Point out every Plasmodium parasite.
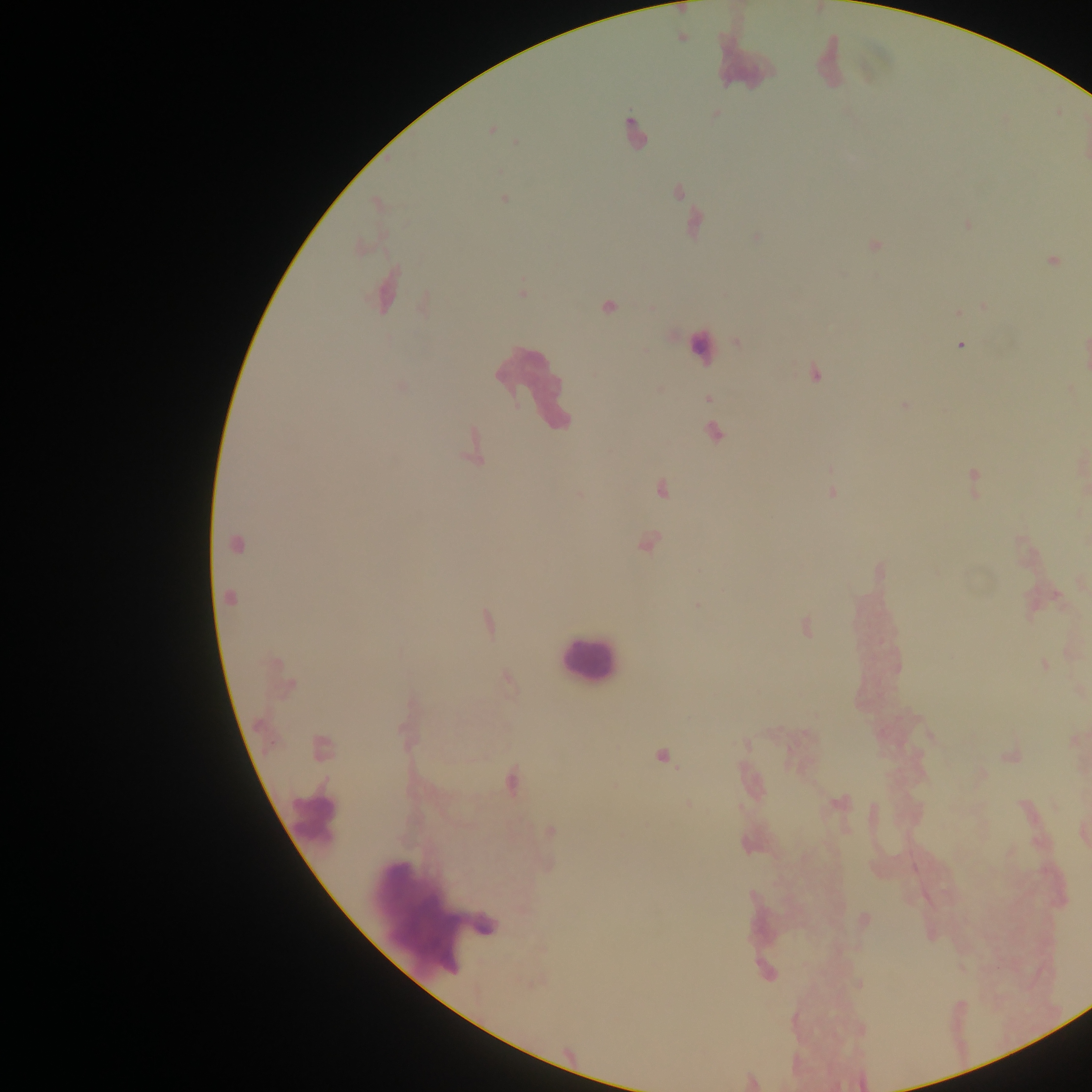
Approximate centers as [x, y] in pixels.
Plasmodium parasites: [492, 130], [504, 198], [1053, 261], [958, 312], [960, 345], [815, 373], [708, 399], [714, 433], [973, 482], [661, 487], [647, 543], [236, 544], [879, 572], [229, 597], [696, 606], [488, 623], [806, 626], [1045, 665], [323, 747], [663, 757], [511, 780], [550, 832].

image size = 1092×1092 pixels
field of view = single
leukocyte locations = approximate centers as [x, y] in pixels: [742, 58], [831, 60], [633, 134], [701, 347], [536, 386], [587, 661], [313, 819], [431, 909]
country = Ghana
capture = mobile-phone photograph through a microscope
preparation = thick blood film